Locate every Plasmodium parasite.
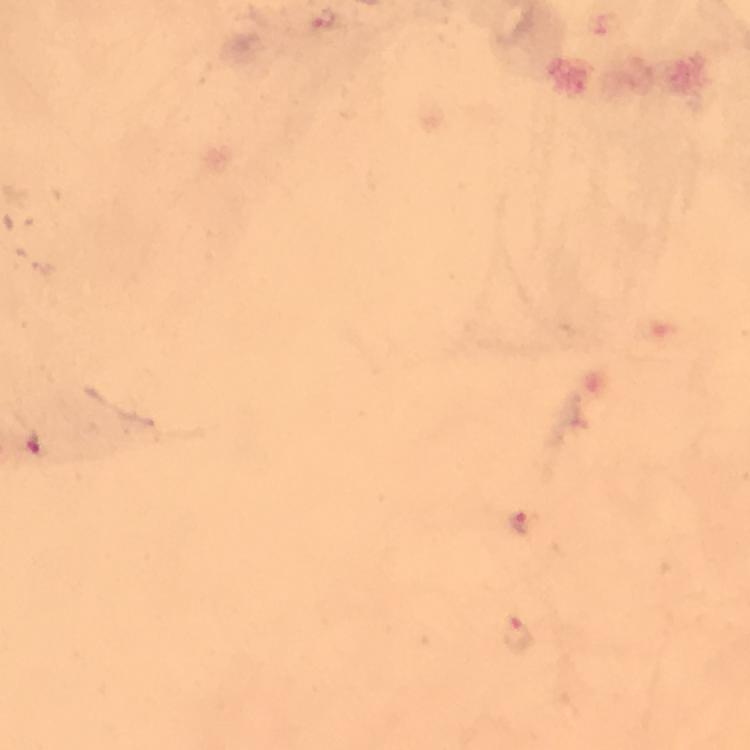

Approximate centers as (x, y) in pixels.
Plasmodium parasites: (321, 20), (40, 445), (519, 523), (520, 634).

100x magnification. From a diagnostic examination for malaria. Thick smear. Image is 750×750 pixels. A crop from one field of view. Photographed through the microscope with a smartphone camera. Immersion oil applied. Giemsa stain.